Identify the parasite.
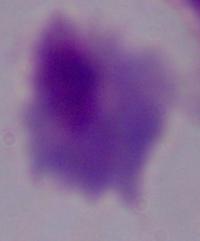
A trichomonad.

Micrograph. Captured at 1000x magnification.